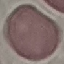

malaria status = uninfected
image type = cell patch, automatically extracted from a larger field of view and resized to 64 × 64 pixels
capture = smartphone through the microscope eyepiece
stain = Giemsa
preparation = thin blood film